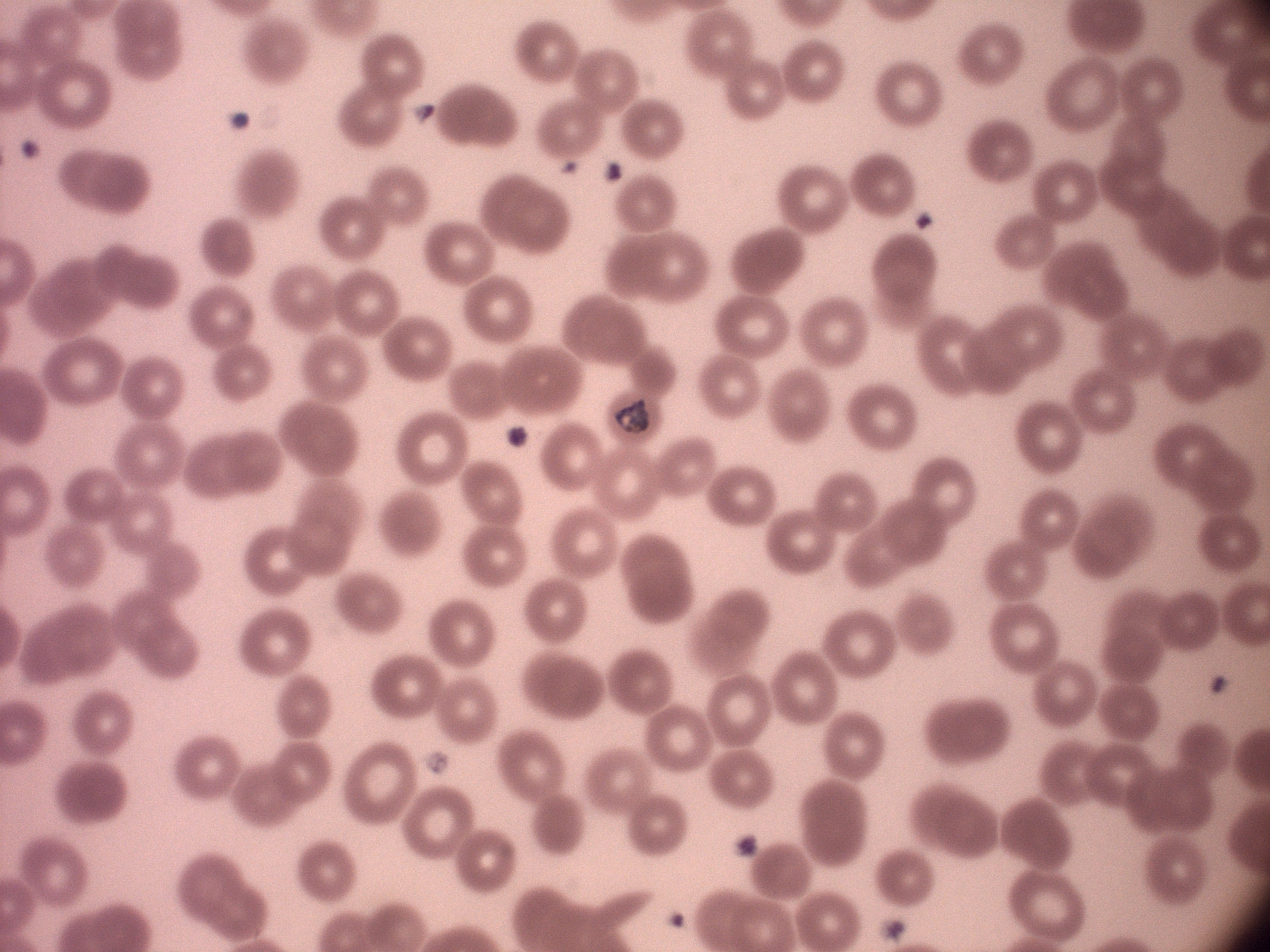

microscope = Leica DM2000 with built-in camera
field of view = single
preparation = thin blood film
image size = 1270×952 pixels
species = Plasmodium malariae
magnification = 100x
stain = Giemsa
trophozoite locations = approximate bounding boxes as [x1, y1, x2, y2] in pixels, from the source annotation, which is not necessarily exhaustive: [613, 399, 652, 433]